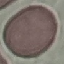

Malaria status: uninfected. Photographed with a smartphone camera at the microscope eyepiece. Giemsa-stained preparation. Thin blood smear. Automatically extracted cell patch, resized to 64 × 64 pixels.